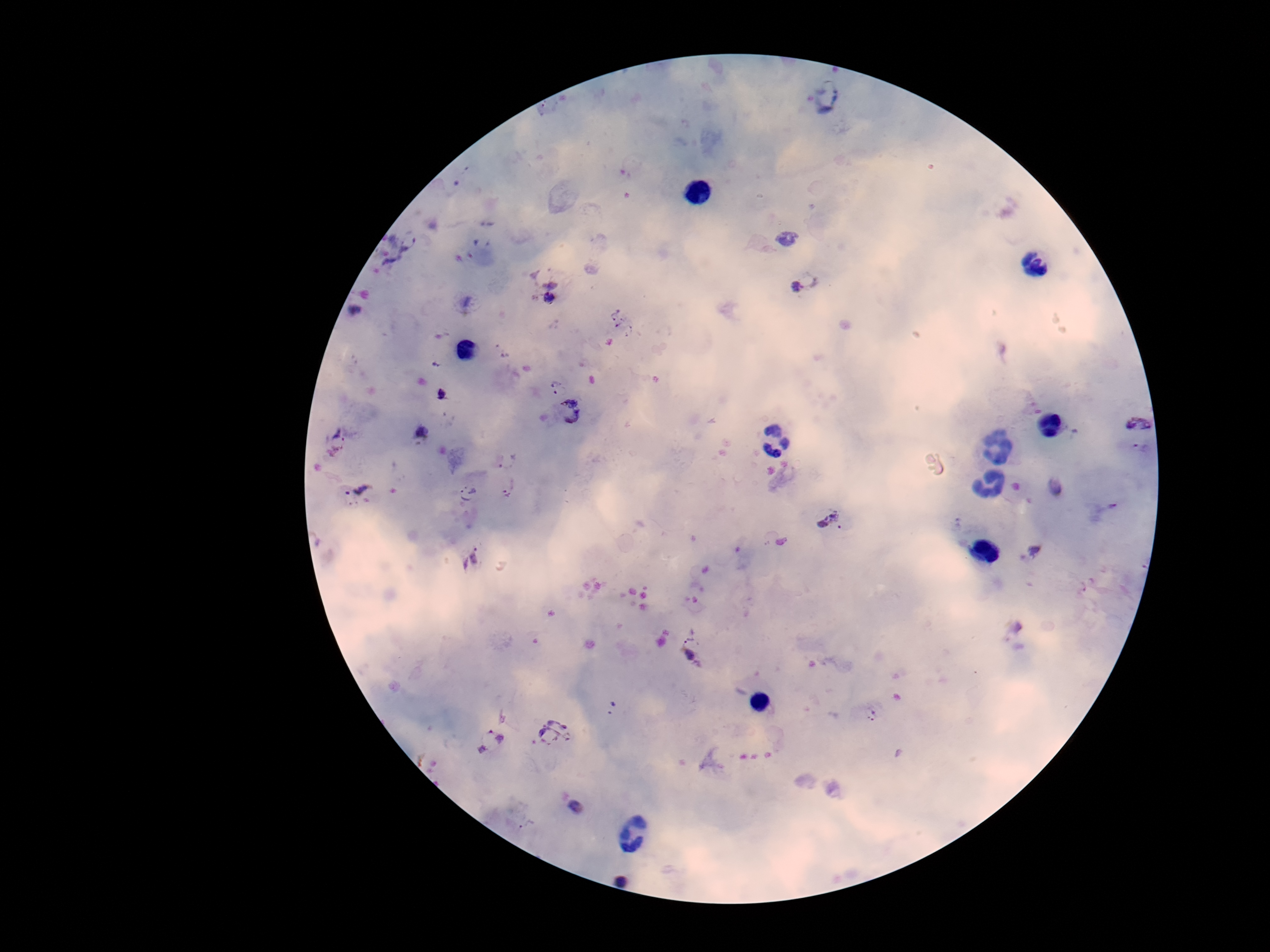 Approximate centers as (x, y) in pixels. Plasmodium parasite locations: (826, 94), (785, 239), (410, 242), (552, 269), (807, 281), (549, 298), (354, 308), (619, 318), (437, 363), (554, 381), (561, 393), (442, 394), (569, 411), (1138, 423), (423, 434), (338, 439), (1141, 449), (506, 456), (509, 487), (360, 488), (1054, 488), (470, 495), (828, 519), (1033, 551), (472, 559), (694, 648), (611, 709), (873, 715), (552, 732), (491, 741), (576, 806), (529, 828), (624, 872). Giemsa-stained preparation. Single field of view. 100x magnification. Image is 1270×952 pixels. Photographed through the microscope eyepiece with a smartphone camera. Thick blood smear. Patient malaria status: positive.